Look for Plasmodium parasites.
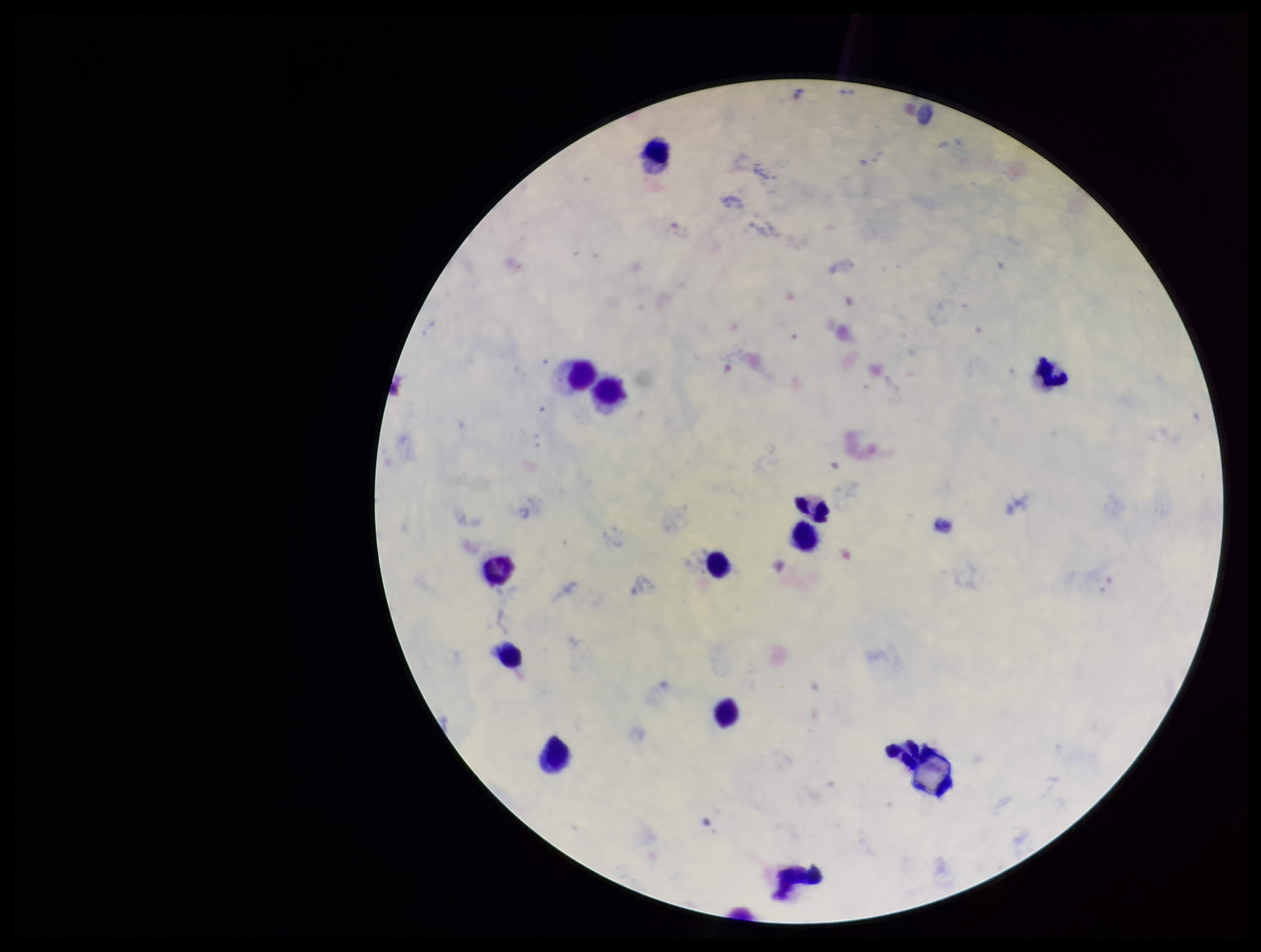

None seen.

Patient malaria status: positive. Single field of view. Parasite count: 0. Smartphone photograph taken through the eyepiece of a microscope. Image is 1261×952 pixels. Giemsa stain. Preparation: thick. Species reported for this patient: Plasmodium vivax. Leukocyte count: 12.